Classify this cell by malaria status.
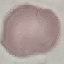

It is uninfected.

Summary:
  - Capture: smartphone camera at the microscope eyepiece
  - Image type: cell patch, automatically extracted from a larger field of view and resized to 64 × 64 pixels
  - Stain: Giemsa
  - Preparation: thin blood smear